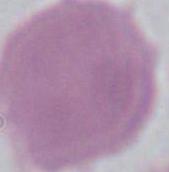

magnification: 1000x
identification: erythrocyte
modality: photomicrograph